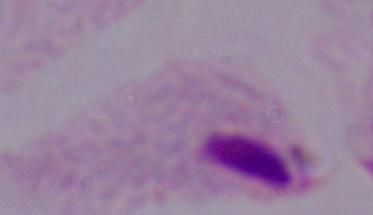
magnification = 1000x
modality = micrograph
identification = trichomonad